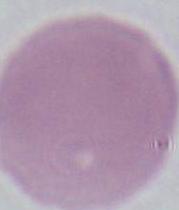
magnification = 1000x
modality = micrograph
identification = erythrocyte